Report the malaria status of this cell.
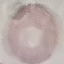

It is uninfected.

capture: smartphone through the microscope eyepiece
preparation: thin smear
stain: Giemsa
image_type: cell patch, automatically extracted from a larger field of view and resized to 64 × 64 pixels